Classify this cell by malaria status.
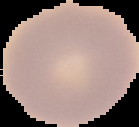
Uninfected.

Image is 139×127 pixels. From a thin blood smear. Segmented cell region on a black background.